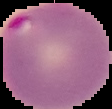 From a thin blood film. Image is 112×109 pixels. Cell region segmented out of the field of view; the surrounding area is masked to black. Result: malaria parasites identified.